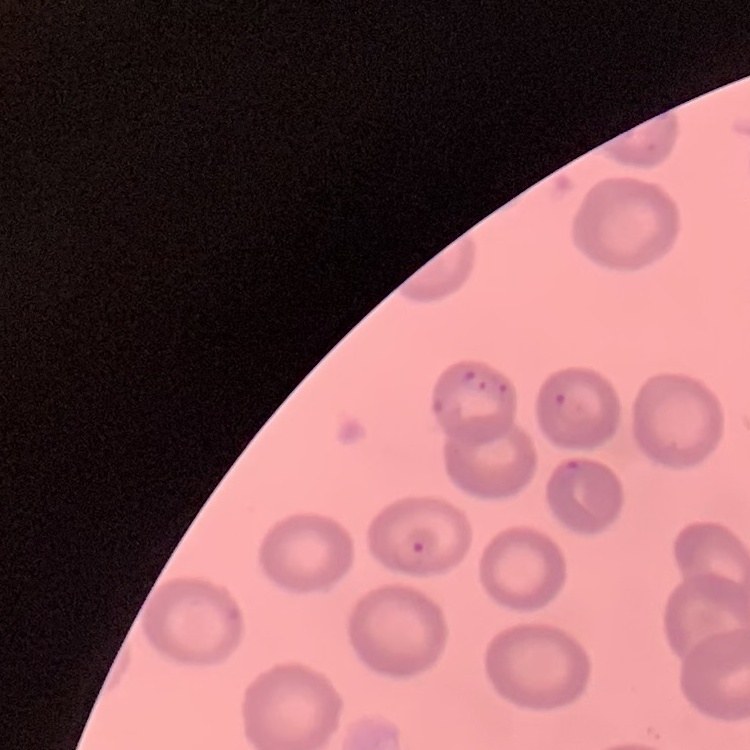

The red blood cells show no rouleaux formation. Stained with either Field's or Giemsa. One tile cut from a larger photomicrograph. Thin blood smear.